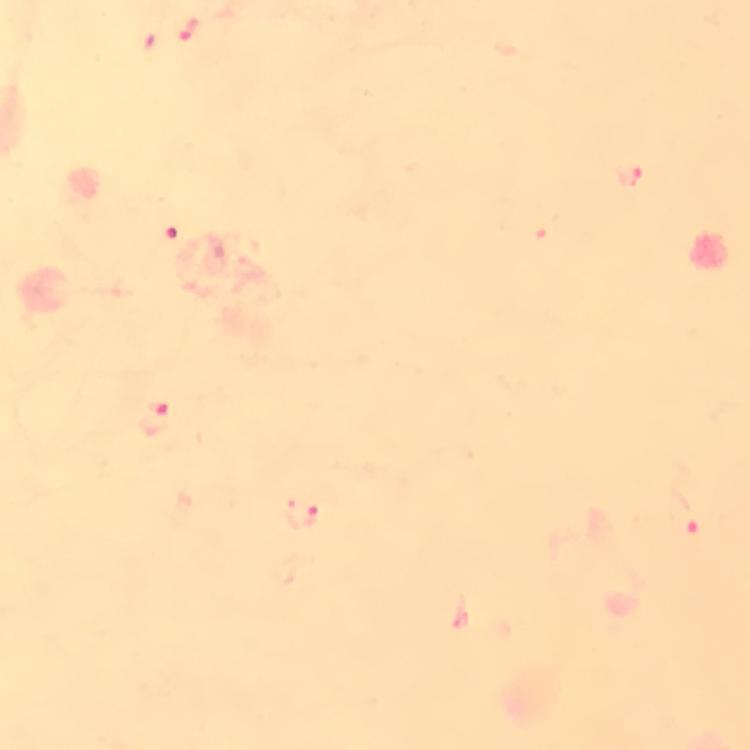

Approximate centers as {x, y} in pixels.
Summary:
  - Malaria parasite locations: {189, 27}, {631, 176}, {171, 231}, {153, 419}, {683, 512}, {301, 514}
  - Magnification: 100x
  - Cropped from: a single field of view
  - Image size: 750×750 pixels
  - Immersion oil: applied
  - Preparation: thick smear
  - Capture: smartphone mounted on the microscope
  - Stain: Giemsa
  - Context: from a diagnostic examination for malaria